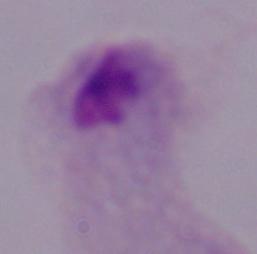
Summary:
  - Identification: trichomonad
  - Modality: micrograph
  - Magnification: 1000x